Classify this cell by malaria status.
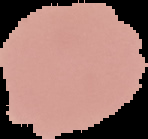
It is uninfected.

Image is 148×139 pixels. From a thin blood film. The area outside the segmented cell region is set to black.